Give the position of every malaria parasite.
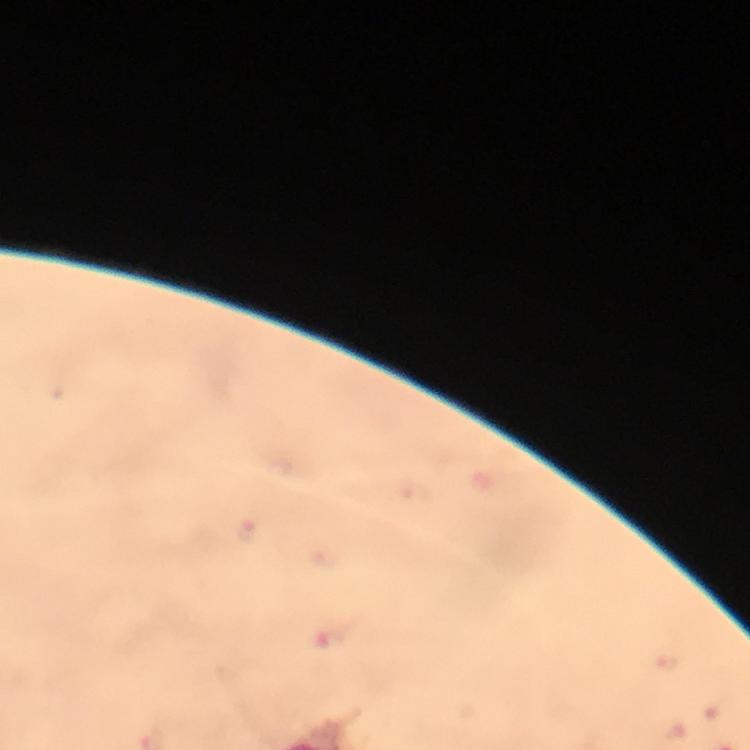
Approximate centers as (x, y) in pixels.
Malaria parasites: (419, 497), (245, 532), (330, 636), (668, 663).

Summary:
  - Context: from a diagnostic examination for malaria
  - Cropped from: a single field of view
  - Immersion oil: applied
  - Preparation: thick blood smear
  - Image size: 750×750 pixels
  - Capture: smartphone photograph through a microscope
  - Stain: Giemsa
  - Magnification: 100x